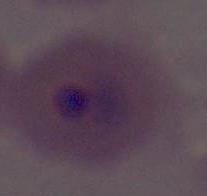

modality = micrograph
identification = Plasmodium
magnification = 400x or 1000x